State which parasite is depicted.
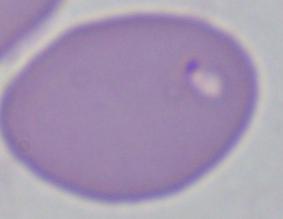
Babesia.

Captured at 1000x magnification. Micrograph.